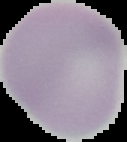
From a thin blood film. Segmented cell region on a black background. Result: no malaria parasites seen. Image is 127×142 pixels.